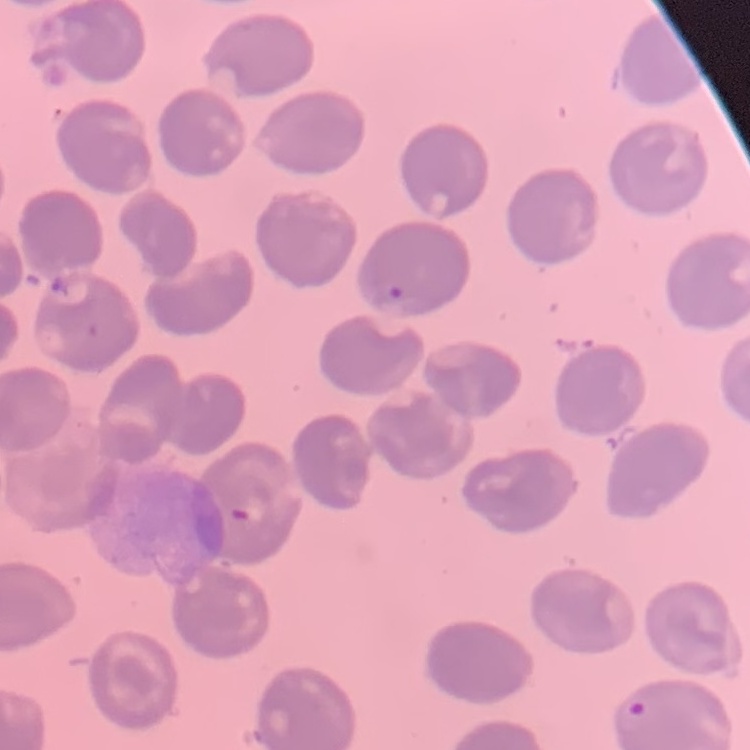
erythrocyte_morphology: no rouleaux formation
stain: Field's or Giemsa
image_type: square crop of a larger photomicrograph
preparation: thin blood smear